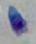
Summary:
  - Modality: photomicrograph
  - Magnification: 1000x
  - Identification: Toxoplasma gondii